Identify the blood parasite species.
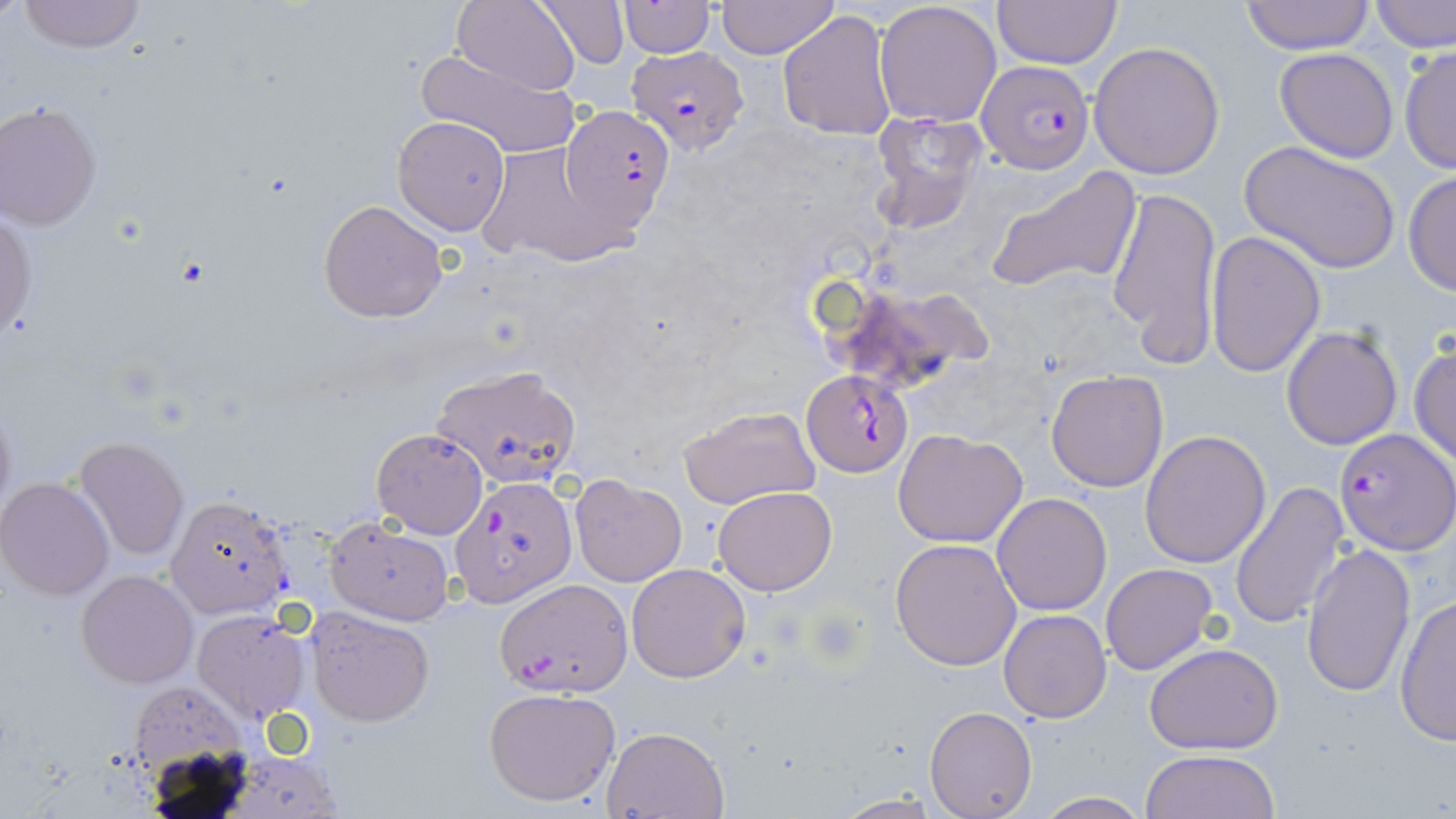
Plasmodium falciparum.

{
  "uninfected_red_blood_cell_locations": "approximate bounding boxes as (x1,y1)-(x2,y2) corner pairs in pixels: (16,0)-(147,53), (453,0)-(583,94), (534,0)-(628,67), (714,0)-(839,59), (1369,0)-(1456,53), (619,1)-(714,56), (874,1)-(1003,126), (991,1)-(1124,69), (1238,1)-(1376,54), (777,9)-(897,141), (1087,40)-(1227,180), (1399,44)-(1456,177), (416,45)-(581,159), (1274,47)-(1400,163), (0,101)-(103,229), (869,110)-(989,235), (392,115)-(511,235), (1240,140)-(1400,274), (474,141)-(622,266), (985,165)-(1142,297), (1403,171)-(1456,296), (1106,182)-(1222,365), (318,200)-(448,322), (0,212)-(37,341), (1204,230)-(1327,378), (826,278)-(994,393), (1280,323)-(1404,450), (1410,342)-(1456,467), (430,364)-(581,487), (1045,369)-(1169,493), (677,405)-(821,511), (372,427)-(488,539), (894,427)-(1027,548), (1140,429)-(1272,568), (76,437)-(189,560), (569,472)-(688,587), (0,477)-(114,600), (1230,480)-(1352,631), (713,486)-(837,595), (991,492)-(1112,615), (164,493)-(293,619), (322,518)-(454,625), (891,539)-(1022,670), (1300,541)-(1417,698), (625,563)-(752,683), (1101,563)-(1218,675), (76,570)-(199,689), (1393,595)-(1456,746), (306,606)-(434,727), (193,610)-(311,722), (998,610)-(1111,723), (1143,642)-(1285,753), (134,683)-(245,798), (483,686)-(622,807), (925,706)-(1037,818), (601,724)-(730,818), (1140,749)-(1280,819), (225,755)-(345,819), (1032,791)-(1151,818), (830,793)-(945,818)",
  "field_of_view": "one of a larger specimen",
  "image_size": "1456×819 pixels",
  "modality": "optical microscopy",
  "magnification": "1000x",
  "stain": "May-Grünwald-Giemsa",
  "preparation": "thin blood film",
  "plasmodium_falciparum_infected_red_blood_cell_locations": "approximate bounding boxes as (x1,y1)-(x2,y2) corner pairs in pixels: (624,44)-(748,155), (975,59)-(1094,173), (559,105)-(677,228), (801,368)-(913,477), (1333,427)-(1454,554), (452,475)-(575,606), (494,577)-(633,696)"
}